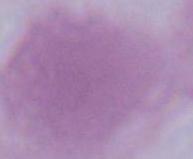
Summary:
  - Identification: red blood cell
  - Magnification: 1000x
  - Modality: photomicrograph